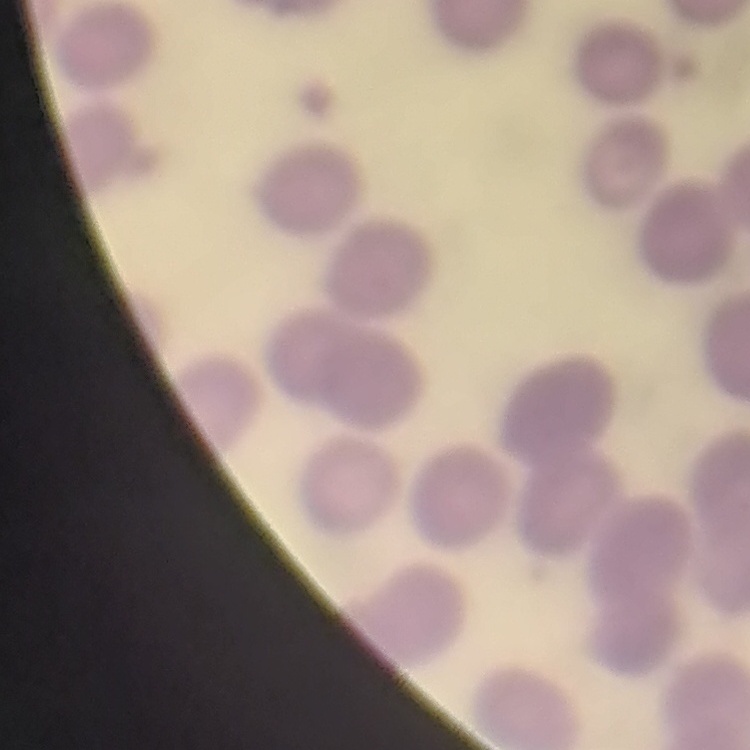 The erythrocytes exhibit no rouleaux formation. One tile cut from a larger photomicrograph. Field's or Giemsa stain. Thin peripheral smear.